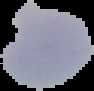
{
  "image_size": "94×91 pixels",
  "preparation": "thin blood film",
  "image_type": "cell region segmented out of the field of view; surrounding area masked to black",
  "result": "no Plasmodium parasites seen"
}